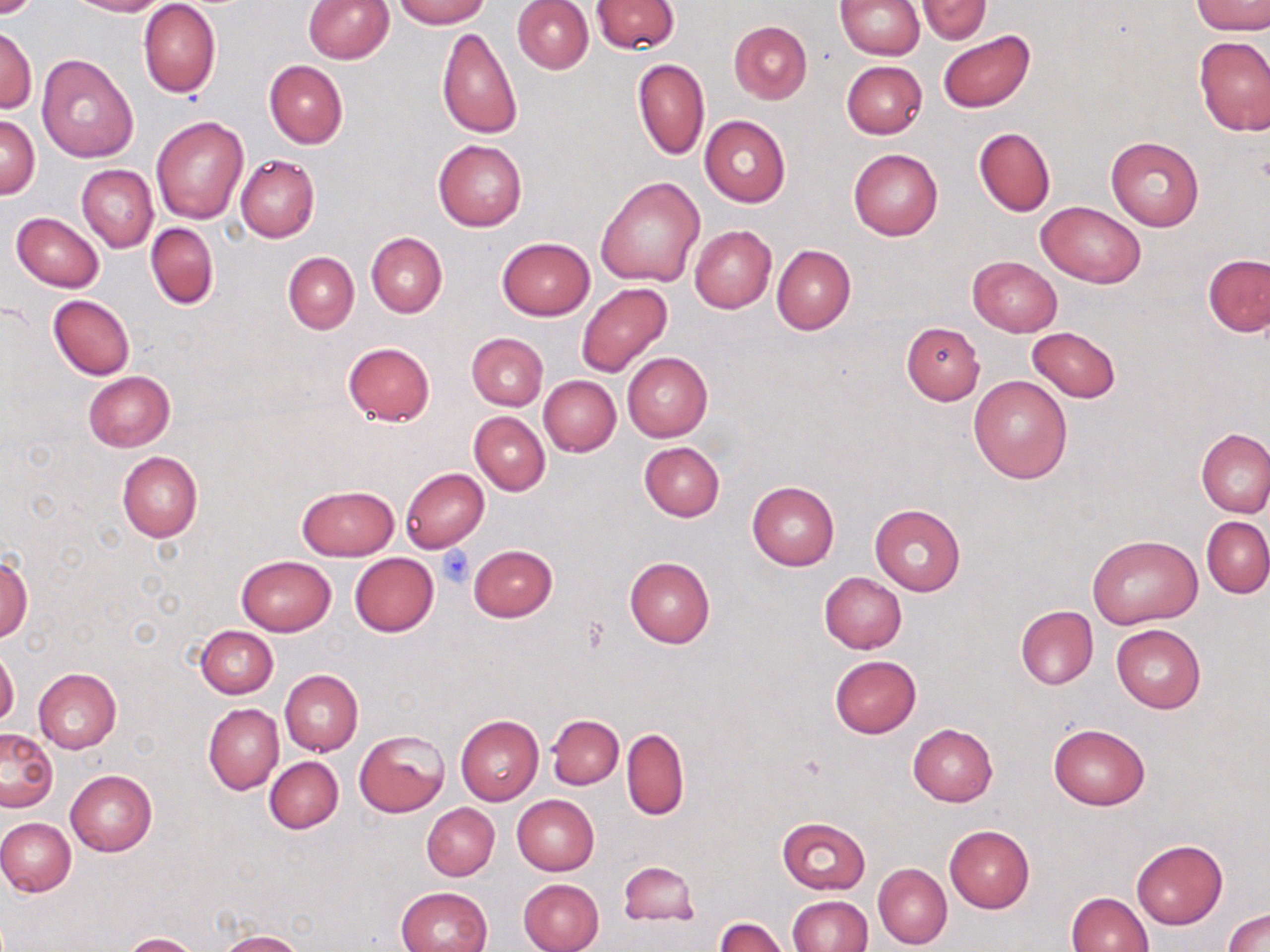

Approximate bounding boxes as named x1/y1/x2/y2 corners in pixels. Platelet locations: (x1=438, y1=547, x2=474, y2=587). Uninfected red blood cell locations: (x1=0, y1=0, x2=45, y2=19), (x1=69, y1=0, x2=167, y2=16), (x1=303, y1=0, x2=395, y2=63), (x1=393, y1=0, x2=489, y2=27), (x1=591, y1=0, x2=680, y2=53), (x1=835, y1=0, x2=924, y2=59), (x1=915, y1=0, x2=992, y2=42), (x1=512, y1=1, x2=593, y2=73), (x1=1190, y1=1, x2=1270, y2=34), (x1=139, y1=2, x2=220, y2=99), (x1=729, y1=21, x2=812, y2=103), (x1=1, y1=24, x2=37, y2=114), (x1=436, y1=26, x2=523, y2=139), (x1=937, y1=30, x2=1035, y2=113), (x1=1194, y1=36, x2=1270, y2=135), (x1=36, y1=53, x2=140, y2=160), (x1=632, y1=59, x2=709, y2=160), (x1=264, y1=60, x2=347, y2=148), (x1=841, y1=60, x2=928, y2=139), (x1=1, y1=115, x2=39, y2=199), (x1=700, y1=115, x2=790, y2=206), (x1=151, y1=116, x2=248, y2=223), (x1=973, y1=127, x2=1056, y2=216), (x1=1106, y1=137, x2=1203, y2=231), (x1=433, y1=139, x2=527, y2=231), (x1=848, y1=147, x2=943, y2=241), (x1=235, y1=154, x2=320, y2=242), (x1=77, y1=165, x2=158, y2=253), (x1=596, y1=175, x2=706, y2=286), (x1=1037, y1=201, x2=1145, y2=289), (x1=12, y1=212, x2=103, y2=291), (x1=146, y1=223, x2=218, y2=310), (x1=689, y1=226, x2=776, y2=312), (x1=366, y1=232, x2=446, y2=316), (x1=496, y1=237, x2=596, y2=320), (x1=772, y1=244, x2=856, y2=335), (x1=283, y1=252, x2=358, y2=333), (x1=1202, y1=253, x2=1270, y2=337), (x1=967, y1=256, x2=1062, y2=336), (x1=576, y1=282, x2=671, y2=376), (x1=48, y1=295, x2=134, y2=380), (x1=900, y1=321, x2=984, y2=406), (x1=1028, y1=326, x2=1121, y2=403), (x1=465, y1=333, x2=548, y2=410), (x1=342, y1=341, x2=435, y2=426), (x1=622, y1=352, x2=712, y2=441), (x1=84, y1=370, x2=174, y2=451), (x1=969, y1=375, x2=1073, y2=484), (x1=538, y1=376, x2=620, y2=457), (x1=469, y1=411, x2=550, y2=495), (x1=1197, y1=429, x2=1270, y2=517), (x1=639, y1=441, x2=724, y2=520), (x1=117, y1=451, x2=202, y2=542), (x1=400, y1=466, x2=490, y2=553), (x1=747, y1=481, x2=839, y2=570), (x1=297, y1=484, x2=398, y2=561), (x1=869, y1=503, x2=966, y2=596), (x1=1202, y1=517, x2=1270, y2=597), (x1=1088, y1=533, x2=1203, y2=629), (x1=468, y1=544, x2=557, y2=622), (x1=0, y1=553, x2=33, y2=641), (x1=349, y1=553, x2=438, y2=637), (x1=236, y1=556, x2=336, y2=635), (x1=624, y1=556, x2=715, y2=647), (x1=819, y1=572, x2=907, y2=653), (x1=1015, y1=606, x2=1098, y2=690), (x1=1112, y1=623, x2=1206, y2=713), (x1=196, y1=625, x2=277, y2=698), (x1=0, y1=647, x2=19, y2=728), (x1=830, y1=655, x2=922, y2=738), (x1=33, y1=668, x2=121, y2=753), (x1=280, y1=669, x2=363, y2=755), (x1=203, y1=703, x2=283, y2=794), (x1=455, y1=715, x2=543, y2=805), (x1=547, y1=715, x2=623, y2=789), (x1=1048, y1=722, x2=1150, y2=811), (x1=908, y1=724, x2=998, y2=807), (x1=0, y1=728, x2=58, y2=813), (x1=622, y1=728, x2=689, y2=820), (x1=355, y1=730, x2=449, y2=817), (x1=265, y1=756, x2=344, y2=833), (x1=65, y1=770, x2=157, y2=856), (x1=512, y1=795, x2=600, y2=875), (x1=422, y1=803, x2=500, y2=881), (x1=0, y1=817, x2=76, y2=896), (x1=776, y1=817, x2=871, y2=894), (x1=944, y1=824, x2=1034, y2=913), (x1=1132, y1=839, x2=1227, y2=929), (x1=617, y1=860, x2=699, y2=927), (x1=873, y1=862, x2=952, y2=950), (x1=518, y1=878, x2=604, y2=952), (x1=396, y1=885, x2=493, y2=952), (x1=1067, y1=891, x2=1153, y2=952), (x1=787, y1=895, x2=872, y2=952), (x1=1223, y1=908, x2=1270, y2=952), (x1=715, y1=917, x2=789, y2=952), (x1=217, y1=930, x2=304, y2=952), (x1=122, y1=933, x2=201, y2=952). Slide-level diagnosis: negative for blood parasites. Captured at 1000x magnification. One field of a larger specimen. Thin blood smear. May-Grünwald-Giemsa stain. Image is 1270×952 pixels. Optical microscopy.